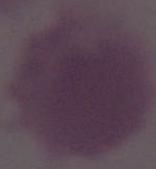

modality = photomicrograph
magnification = 1000x
identification = red blood cell